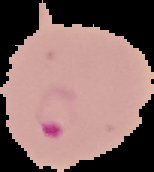 Malaria status: parasitized. From a thin blood smear. Segmented cell region on a black background. Image is 154×172 pixels.